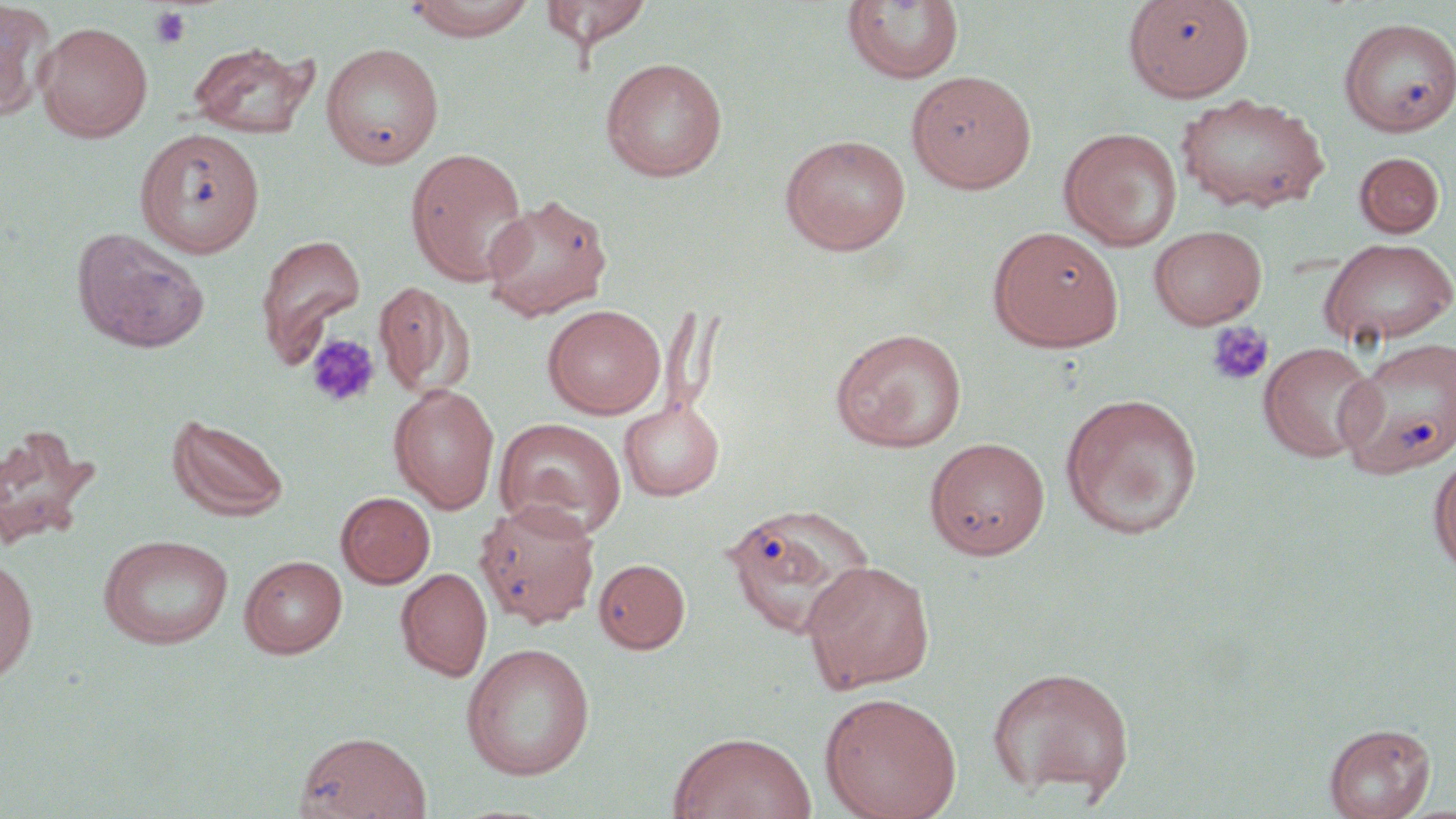
Summary:
  - Coordinate format: approximate bounding boxes as [x1, y1, x2, y2] in pixels
  - Platelet locations (subset): [149, 5, 192, 50], [1205, 321, 1274, 388], [305, 332, 380, 408]
  - Uninfected red blood cell locations (subset): [405, 0, 537, 41], [1122, 0, 1254, 102], [539, 1, 653, 54], [842, 2, 966, 85], [0, 3, 58, 121], [1338, 16, 1456, 137], [36, 22, 153, 142], [187, 40, 318, 139], [320, 42, 444, 168], [600, 57, 728, 182], [905, 70, 1037, 193], [1175, 92, 1329, 214], [135, 127, 265, 258], [1059, 128, 1182, 250], [779, 133, 911, 255], [406, 147, 530, 286], [1354, 151, 1445, 238], [480, 194, 614, 321], [987, 225, 1124, 352], [71, 226, 211, 354], [255, 235, 366, 362], [1317, 238, 1456, 348], [375, 280, 474, 399], [542, 304, 666, 419], [830, 328, 967, 453], [1339, 335, 1455, 478], [1258, 342, 1380, 463], [387, 382, 500, 514], [1058, 392, 1204, 540], [618, 398, 725, 501], [166, 411, 290, 523], [494, 417, 627, 539], [0, 423, 99, 551], [924, 436, 1050, 560], [1428, 452, 1456, 577], [336, 492, 435, 588], [472, 499, 599, 631], [719, 501, 877, 640], [97, 534, 234, 649], [0, 553, 38, 686], [239, 554, 348, 658], [594, 558, 690, 653], [801, 559, 936, 693], [396, 567, 492, 681], [460, 642, 596, 780], [985, 665, 1136, 803], [819, 691, 962, 819], [1323, 722, 1435, 819], [294, 730, 432, 819], [667, 731, 817, 819]
  - Slide-level diagnosis: negative for blood parasites
  - Field of view: single
  - Stain: May-Grünwald-Giemsa
  - Modality: optical microscopy
  - Magnification: 1000x
  - Image size: 1456×819 pixels
  - Preparation: thin blood smear